Assess the morphology of the erythrocytes.
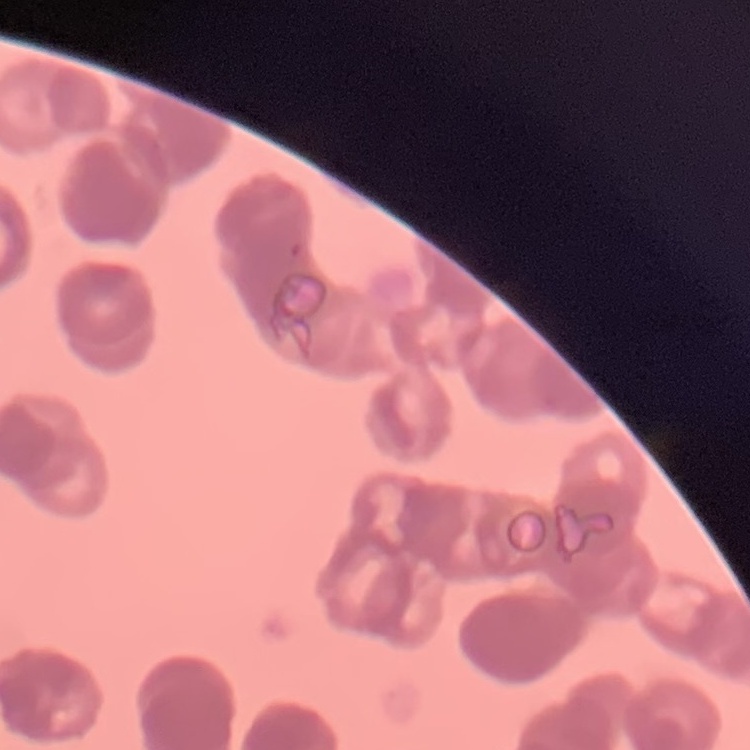

They show rouleaux formation.

One tile cut from a larger photomicrograph. Thin peripheral smear. Stained with either Field's or Giemsa.